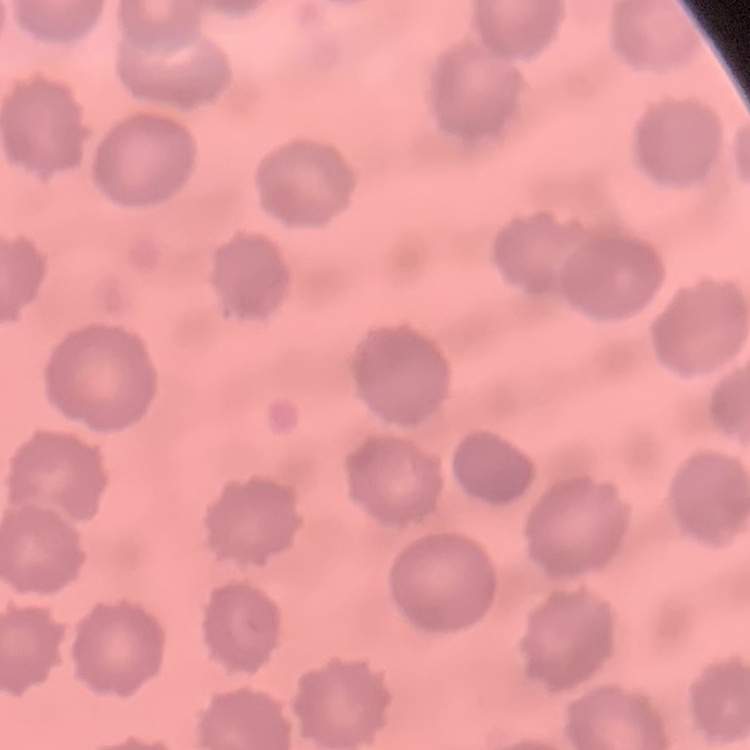

The red blood cells exhibit no rouleaux formation. Square crop of a larger photomicrograph. Stained with either Field's or Giemsa. Thin peripheral smear.